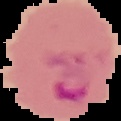
From a thin blood film. Segmented cell region on a black background. Image is 121×121 pixels. Result: Plasmodium parasites detected.